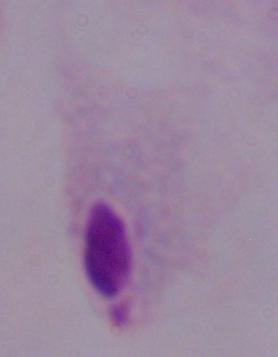
identification: trichomonad
modality: photomicrograph
magnification: 1000x